Locate every uninfected red blood cell.
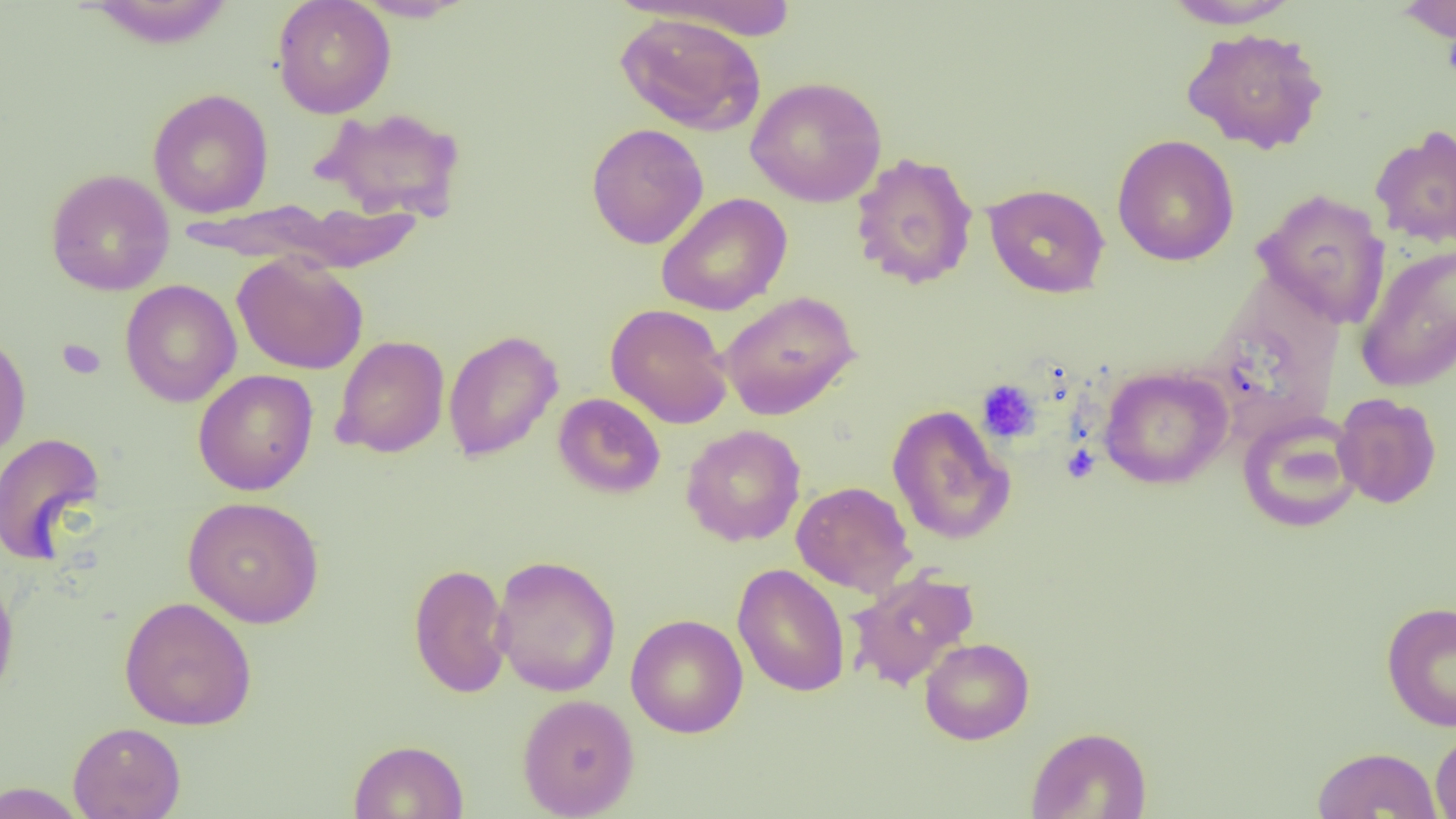
Approximate bounding boxes as (x1,y1)-(x2,y2) corner pairs in pixels.
Uninfected red blood cells: (272,0)-(396,118), (349,0)-(478,22), (1395,0)-(1456,43), (80,1)-(239,49), (632,1)-(806,41), (1162,1)-(1303,29), (615,12)-(767,135), (1181,26)-(1330,155), (746,76)-(887,207), (148,88)-(274,218), (312,106)-(467,223), (586,123)-(709,249), (1369,124)-(1456,249), (1112,135)-(1240,266), (850,152)-(979,290), (45,168)-(175,296), (983,183)-(1110,299), (1253,188)-(1391,328), (655,193)-(793,316), (1355,244)-(1456,393), (232,253)-(369,375), (119,279)-(242,407), (718,290)-(860,420), (605,303)-(733,429), (443,329)-(563,462), (0,331)-(31,462), (332,335)-(450,458), (1098,365)-(1233,489), (192,369)-(319,495), (553,393)-(666,499), (1333,393)-(1442,509), (887,404)-(1015,546), (1237,411)-(1364,533), (680,424)-(806,547), (0,432)-(106,565), (791,481)-(917,597), (182,496)-(325,628), (491,554)-(621,697), (408,562)-(513,699), (732,563)-(850,698), (0,567)-(19,708), (845,569)-(980,692), (118,596)-(257,731), (1380,601)-(1456,732), (625,614)-(748,738), (920,637)-(1034,745), (516,693)-(640,819), (68,721)-(186,819), (1025,726)-(1152,818), (1430,728)-(1456,819), (348,739)-(469,819), (1312,746)-(1442,818), (0,781)-(90,818).

Platelet locations: (57,338)-(105,379), (976,379)-(1041,443), (1062,444)-(1099,484). Slide-level diagnosis: negative for blood parasites. Thin blood film. 1000x magnification. Image is 1456×819 pixels. One field of a larger specimen. Light microscopy.